Report the malaria status of this cell.
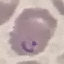
It is parasitized.

Giemsa stain. Photographed with a smartphone camera at the microscope eyepiece. Automatically extracted cell patch, resized to 64 × 64 pixels. Thin blood film.